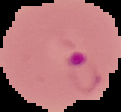

Summary:
  - Malaria status: parasitized
  - Image size: 121×112 pixels
  - Preparation: thin blood film
  - Image type: segmented cell region with the area outside set to black